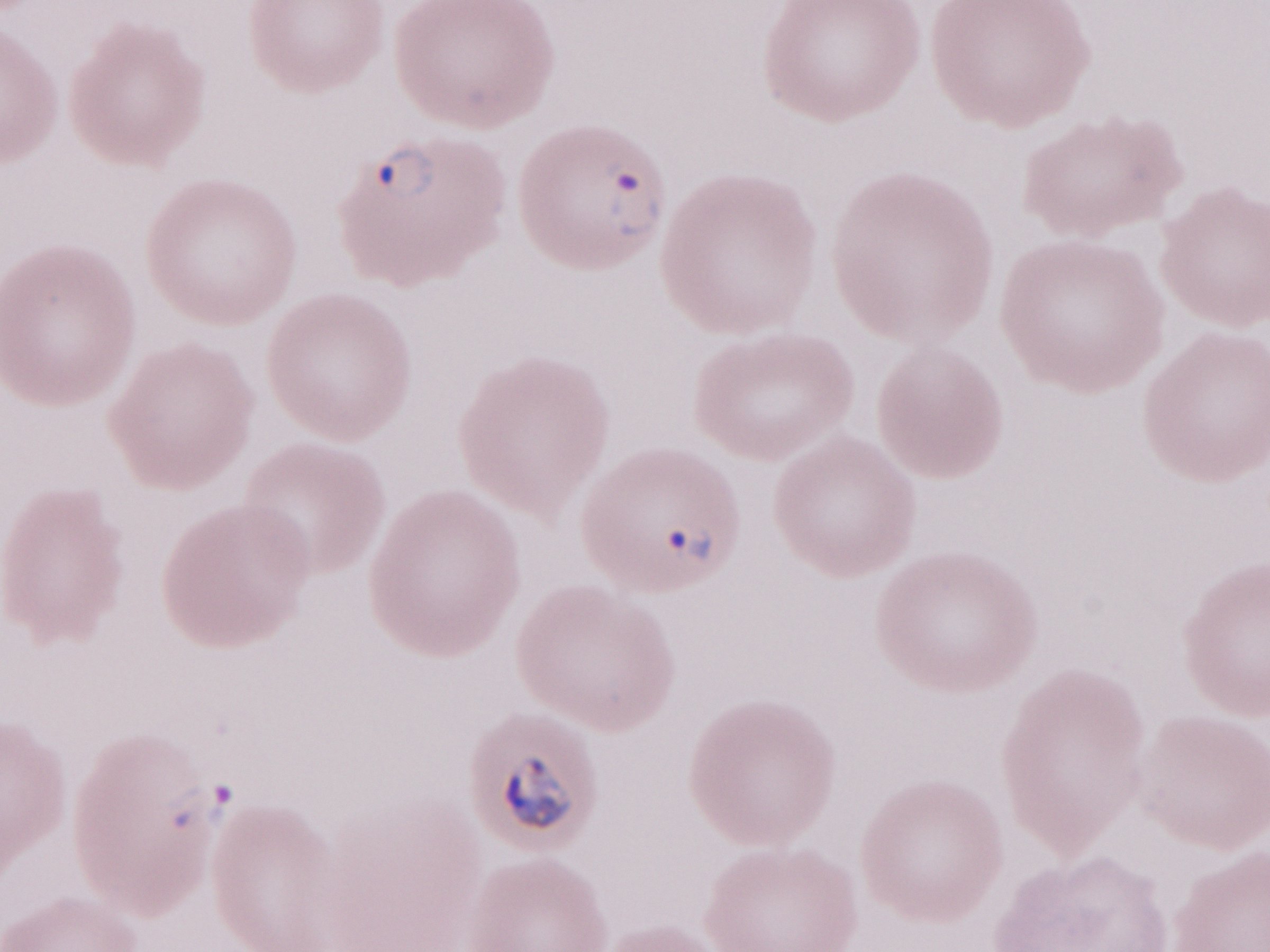

May-Grünwald-Giemsa (MGG) stain. 1,000x magnification. Olympus BX43 microscope, Olympus DP73 camera. Image is 1270×952 pixels. Patient diagnosis: malaria infection. Single field of view. Thin blood film.